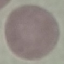

Malaria status: uninfected. Acquired by smartphone through the microscope eyepiece. Thin blood film. Giemsa-stained preparation. Automatically extracted cell patch, resized to 64 × 64 pixels.